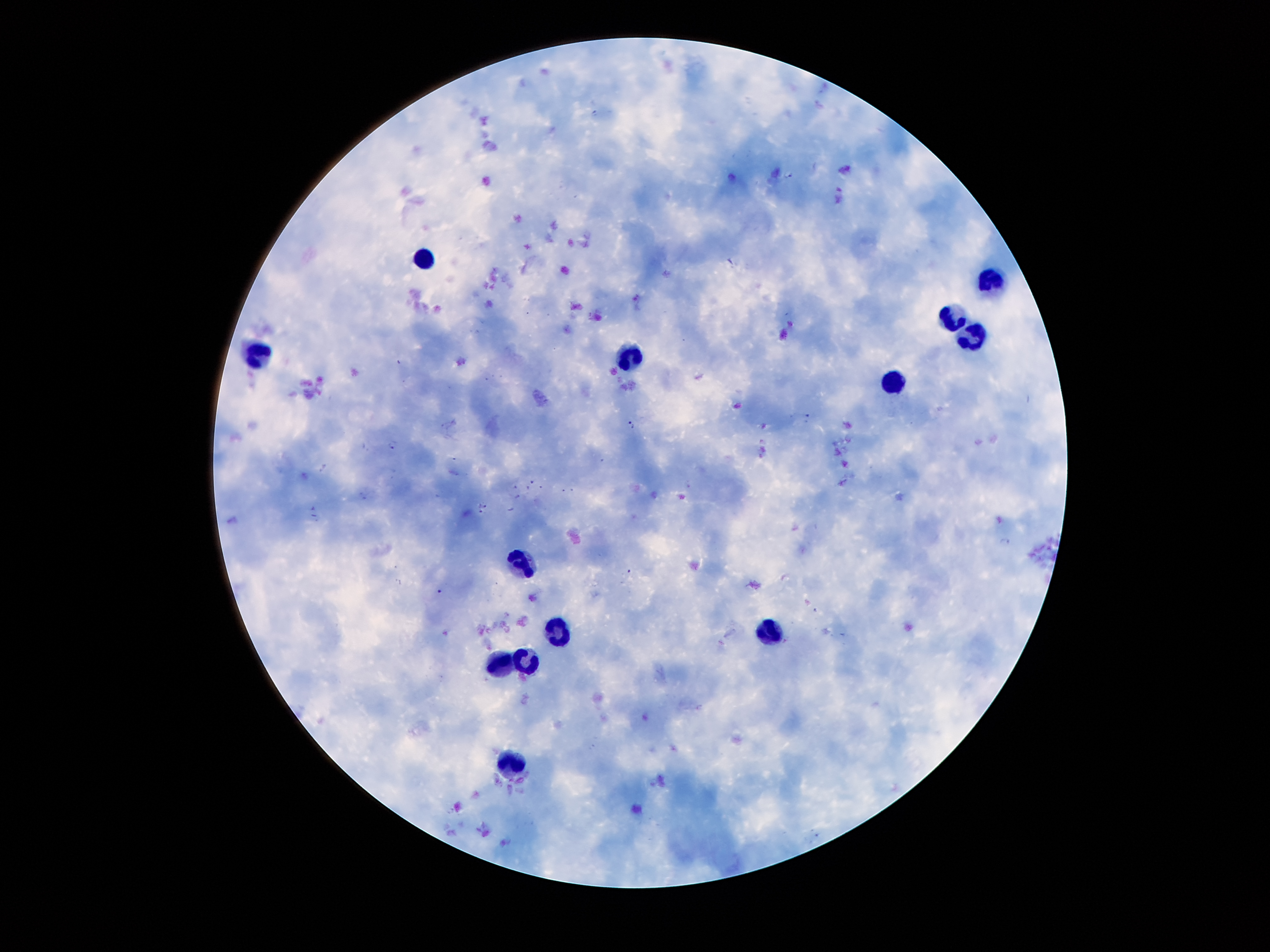

coordinate format = approximate centers as (x, y) in pixels
malaria parasite locations = (790, 175), (809, 418), (631, 425), (392, 443), (517, 495), (483, 505), (480, 511), (1006, 543)
leukocyte locations = (424, 260), (987, 283), (953, 320), (972, 336), (258, 353), (629, 359), (892, 385), (525, 566), (764, 628), (558, 631), (527, 656), (497, 663), (508, 764)
capture = smartphone through the microscope eyepiece
image size = 1270×952 pixels
patient malaria status = positive for Plasmodium falciparum
preparation = thick blood film
field of view = one from this slide
magnification = 100x
stain = Giemsa